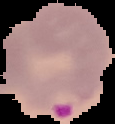
Image is 115×124 pixels. From a thin blood smear. Malaria status: parasitized. Cell region segmented out of the field of view; the surrounding area is masked to black.